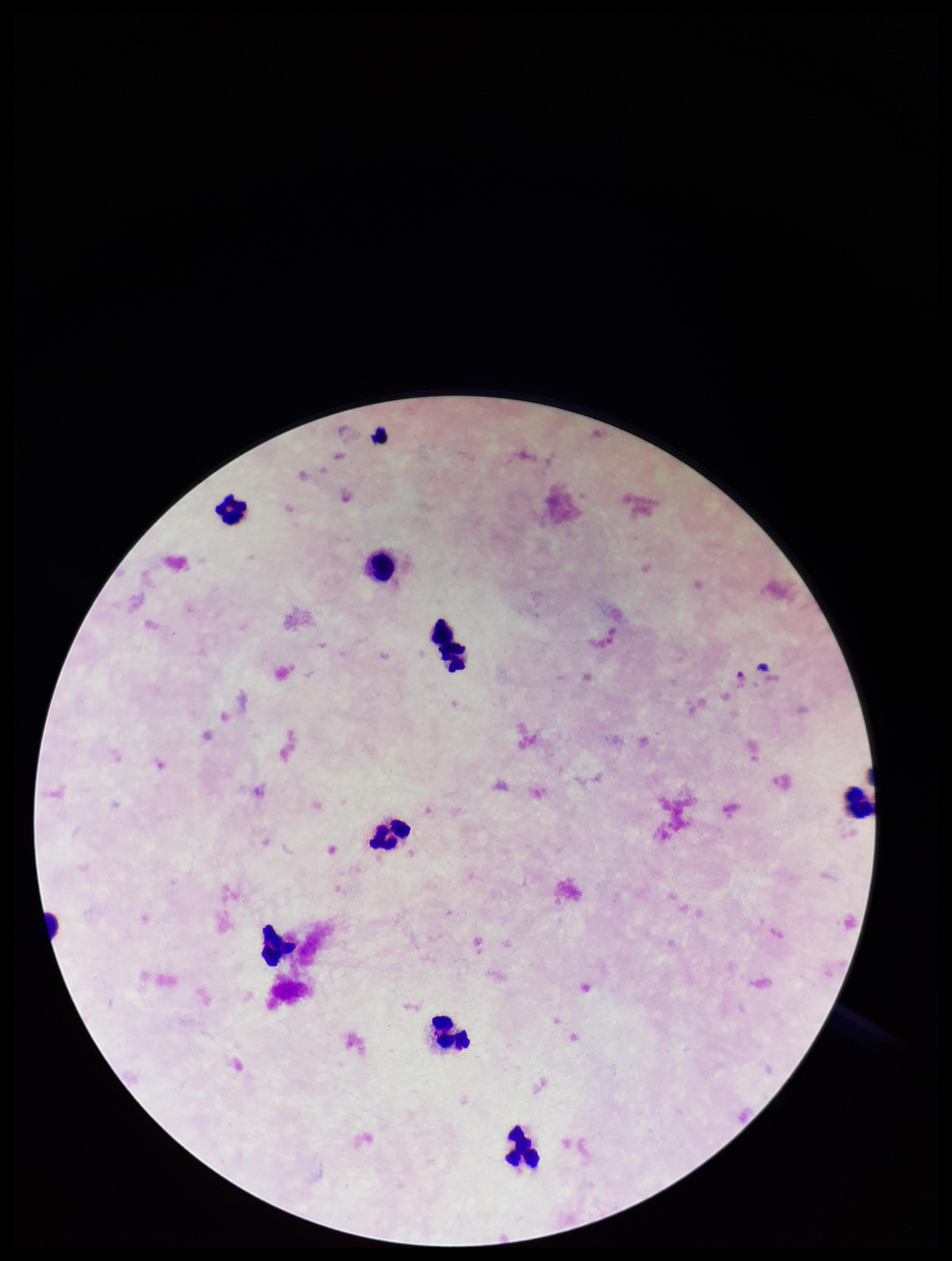
Smartphone photograph taken through the eyepiece of a microscope. Patient malaria status: negative. Stained with Giemsa. Plasmodium parasites: none detected. Single field of view. Preparation: thick blood smear. Image is 952×1261 pixels. Parasite count: 0. Leukocyte count: 8.